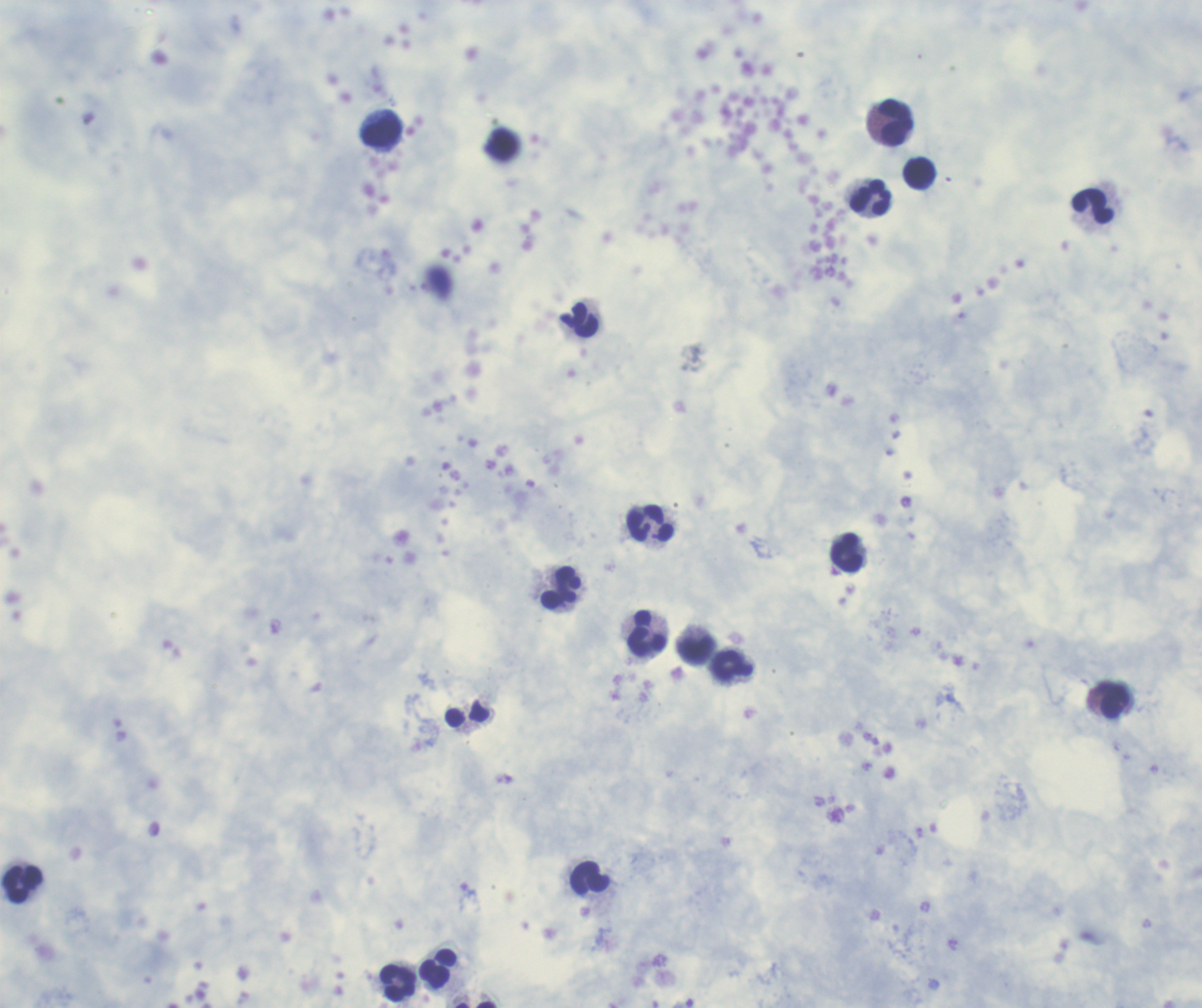
{
  "result": "no Plasmodium parasites seen",
  "stain": "Romanowsky",
  "field_of_view": "single",
  "background_quality": "good",
  "image_size": "1202×1008 pixels",
  "coloration_quality": "good",
  "leukocyte_locations": "approximate centers as {x, y} in pixels: {895, 122}, {382, 132}, {918, 172}, {869, 197}, {1093, 206}, {578, 319}, {651, 523}, {847, 552}, {562, 588}, {647, 632}, {695, 649}, {731, 664}, {1114, 700}, {467, 715}, {590, 877}, {22, 883}, {438, 969}, {397, 983}",
  "magnification": "100x",
  "context": "previously used in a real diagnosis",
  "preparation": "thick smear of blood"
}